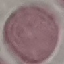
malaria status = uninfected
capture = smartphone through the microscope eyepiece
preparation = thin blood smear
image type = automatically extracted cell patch, resized to 64 × 64 pixels
stain = Giemsa